Classify this cell by malaria status.
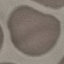
It is uninfected.

Giemsa stain. Acquired by smartphone through the microscope eyepiece. Thin blood film. Automatically extracted cell patch, resized to 64 × 64 pixels.